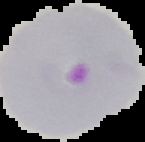

Summary:
  - Result: Plasmodium parasites identified
  - Image type: segmented cell region with the area outside set to black
  - Preparation: thin blood film
  - Image size: 145×142 pixels